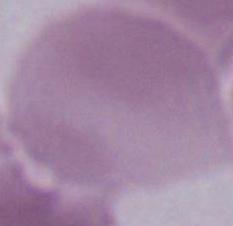

1000x magnification. Photomicrograph. An erythrocyte is shown.